Report the malaria status of this cell.
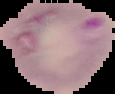
It is parasitized.

image type = segmented cell region with the area outside set to black
image size = 115×94 pixels
preparation = thin blood smear